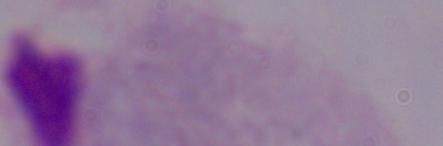

Summary:
  - Identification: trichomonad
  - Magnification: 1000x
  - Modality: photomicrograph